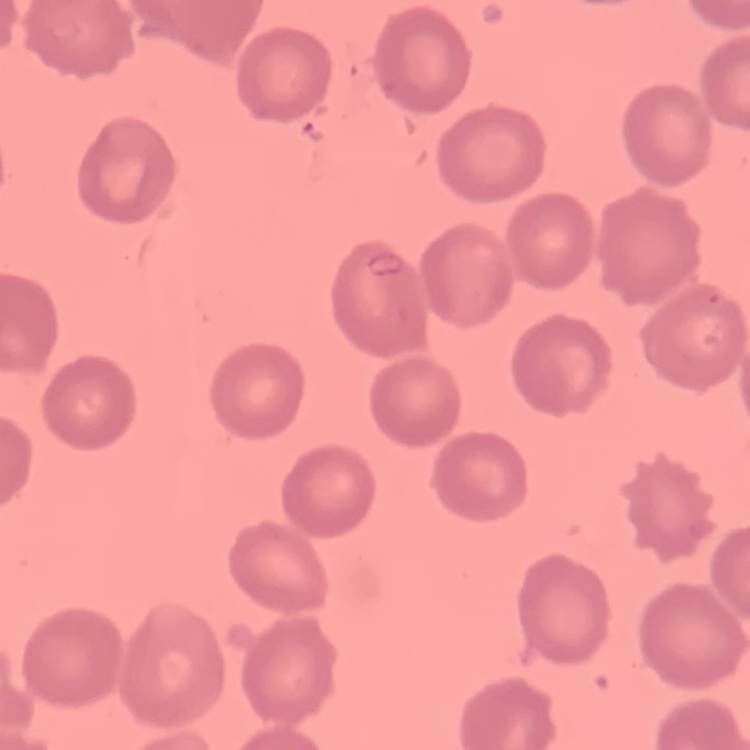

The red blood cells show no rouleaux formation. Square crop of a larger photomicrograph. Stained with either Field's or Giemsa. Thin blood smear.